Report the malaria status of this cell.
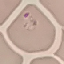
Parasitized.

Thin smear of blood. Photographed with a smartphone camera at the microscope eyepiece. Automatically extracted cell patch, resized to 64 × 64 pixels. Giemsa-stained preparation.